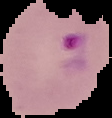
image_size: 112×118 pixels
malaria_status: parasitized
image_type: cell region segmented out of the field of view; surrounding area masked to black
preparation: thin blood smear